Name the parasite shown.
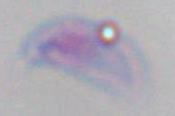
This is Toxoplasma gondii.

Micrograph. 1000x magnification.